State the blood parasite species.
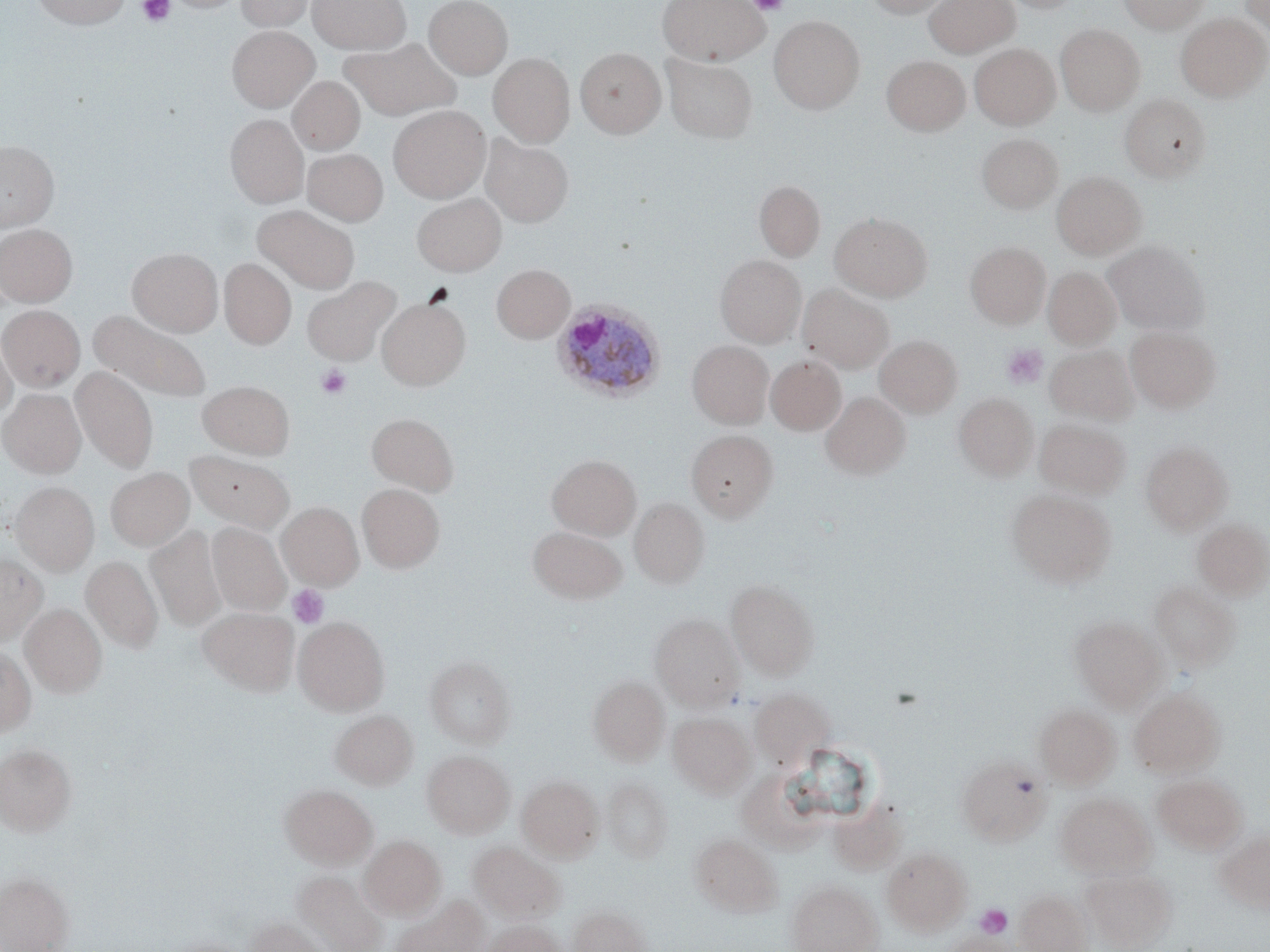
Plasmodium ovale.

Approximate bounding boxes as (x1, y1, x2, y2) in pixels. Uninfected red blood cell locations: (32, 0, 132, 29), (164, 0, 248, 13), (236, 0, 314, 31), (308, 0, 410, 54), (424, 0, 513, 79), (657, 0, 770, 64), (863, 0, 952, 18), (925, 0, 1019, 57), (1000, 0, 1083, 13), (1119, 0, 1208, 32), (1239, 0, 1270, 39), (1176, 13, 1269, 101), (769, 16, 864, 114), (1056, 24, 1145, 114), (227, 25, 319, 111), (340, 37, 461, 122), (969, 43, 1060, 129), (576, 48, 665, 137), (489, 53, 575, 146), (662, 54, 758, 143), (881, 55, 970, 135), (288, 76, 366, 154), (1120, 93, 1209, 182), (389, 105, 490, 202), (225, 114, 308, 207), (481, 133, 573, 227), (977, 133, 1062, 213), (0, 140, 59, 231), (303, 148, 388, 225), (1051, 171, 1146, 259), (754, 181, 825, 260), (412, 193, 506, 276), (253, 205, 360, 292), (830, 212, 932, 301), (0, 224, 77, 307), (1105, 241, 1208, 334), (965, 242, 1051, 328), (128, 248, 223, 335), (715, 254, 806, 345), (220, 258, 296, 348), (492, 264, 574, 343), (1043, 267, 1122, 349), (302, 276, 400, 366), (798, 284, 894, 374), (377, 297, 470, 390), (0, 305, 85, 391), (89, 309, 212, 403), (1125, 326, 1221, 413), (0, 330, 17, 420), (875, 335, 962, 416), (687, 340, 774, 428), (1045, 345, 1138, 423), (766, 355, 846, 435), (71, 366, 158, 471), (198, 381, 294, 458), (0, 389, 86, 478), (821, 392, 910, 479), (954, 393, 1039, 480), (367, 412, 458, 495), (1035, 418, 1130, 498), (687, 430, 777, 521), (1141, 441, 1232, 532), (185, 450, 294, 533), (547, 454, 641, 540), (106, 467, 194, 551), (10, 481, 99, 575), (357, 483, 444, 572), (1006, 488, 1116, 588), (630, 497, 709, 588), (278, 502, 363, 589), (1192, 518, 1270, 599), (207, 522, 290, 616), (527, 525, 627, 603), (146, 526, 226, 631), (0, 554, 47, 647), (81, 555, 162, 653), (726, 578, 819, 679), (1149, 580, 1240, 671), (21, 604, 107, 697), (199, 607, 298, 695), (650, 613, 745, 710), (294, 615, 389, 715), (1070, 615, 1164, 708), (0, 647, 36, 735), (425, 655, 516, 747), (588, 675, 669, 763), (750, 688, 833, 768), (1130, 688, 1225, 777), (1035, 703, 1119, 787), (331, 709, 418, 789), (669, 712, 755, 796), (0, 744, 77, 836), (422, 750, 514, 838), (957, 755, 1050, 843), (735, 772, 832, 863), (1153, 773, 1247, 853), (517, 775, 603, 861), (602, 776, 673, 862), (280, 784, 377, 868), (1055, 792, 1154, 877), (832, 797, 915, 881), (1216, 829, 1270, 911), (691, 832, 783, 917), (360, 835, 446, 919), (469, 840, 564, 922), (882, 846, 972, 934), (1081, 867, 1177, 950), (293, 871, 387, 952), (0, 872, 73, 952), (786, 880, 882, 952), (1015, 888, 1093, 952), (391, 896, 487, 952), (568, 904, 650, 952), (247, 916, 327, 952), (485, 920, 566, 952), (941, 931, 1016, 951), (156, 938, 255, 952). Plasmodium ovale-infected red blood cell locations: (552, 302, 666, 403). Platelet locations: (137, 0, 175, 26), (748, 0, 788, 15), (1001, 343, 1048, 389), (317, 364, 351, 399), (287, 585, 329, 629), (975, 904, 1013, 940). Thin blood film. Light microscopy. Single field of view. Captured at 1000x magnification. May-Grünwald-Giemsa-stained preparation. Image is 1270×952 pixels.